State the preparation type.
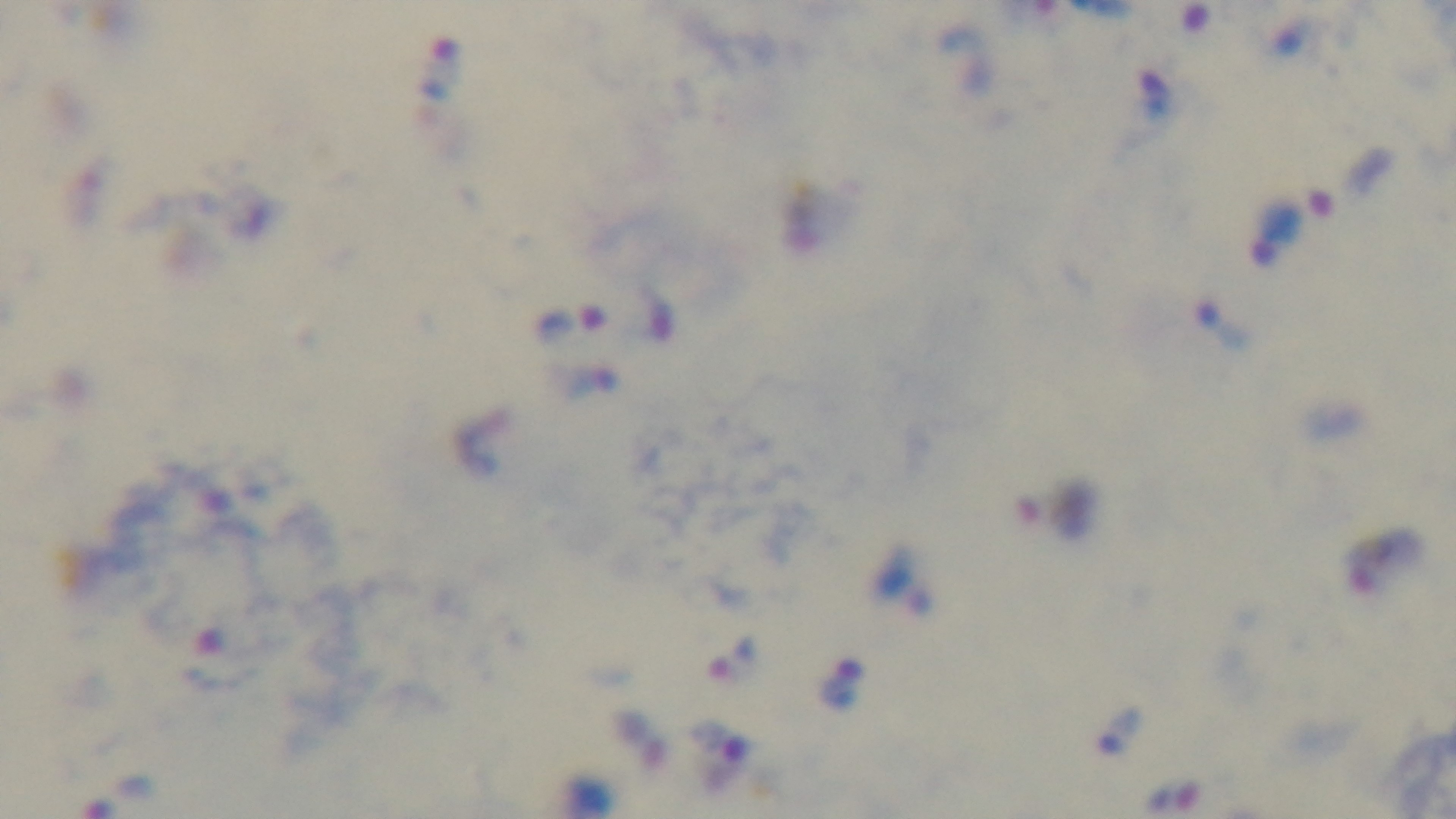

Thick.

objective = 100x oil immersion
capture = mounted 4K digital camera
malaria status = infected
stain = Giemsa
field of view = one from the slide
modality = light microscopy